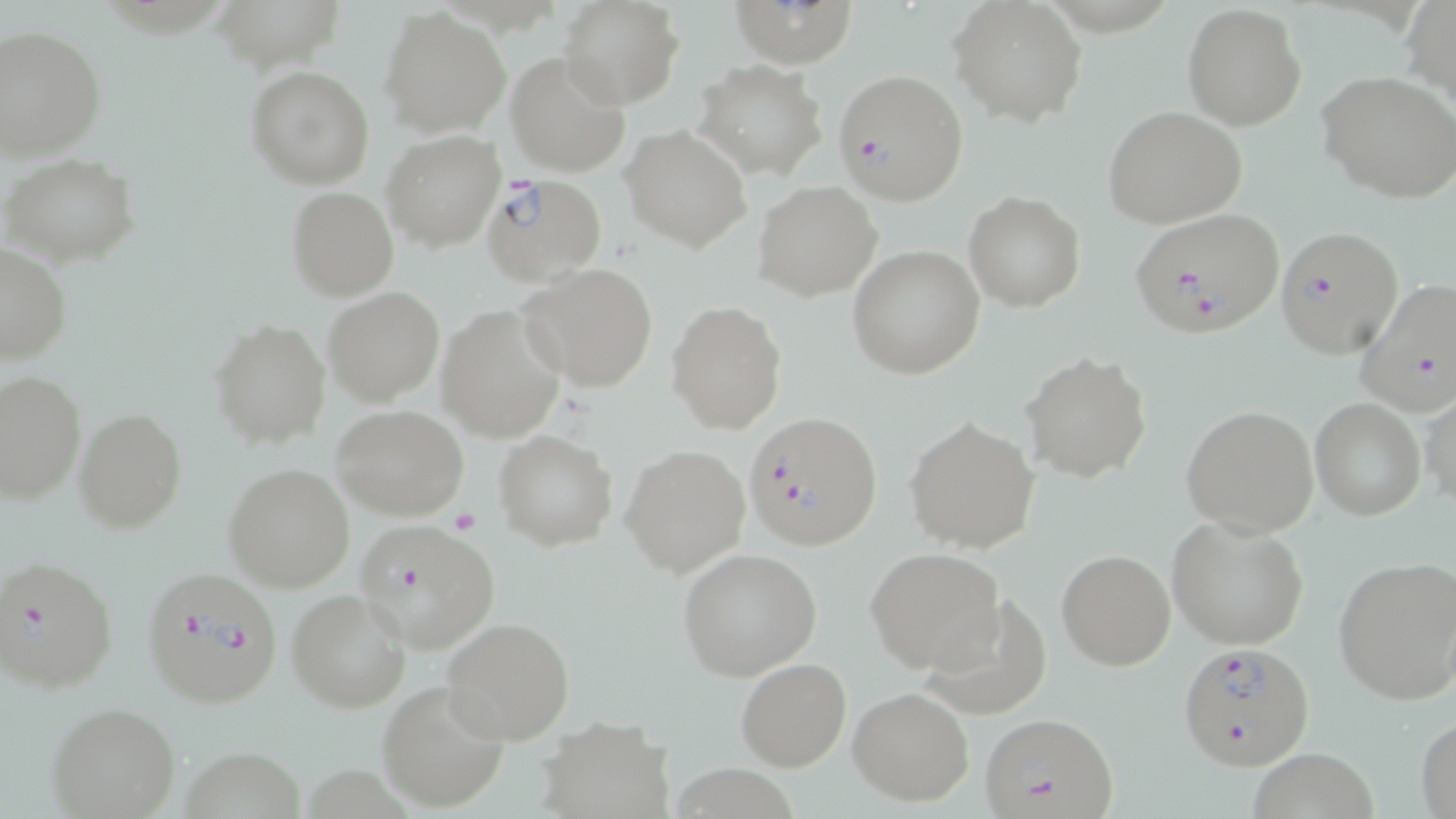

Approximate bounding boxes as [x1, y1, x2, y2] in pixels. Uninfected red blood cell locations: [559, 0, 682, 109], [733, 0, 854, 68], [948, 0, 1088, 128], [1404, 0, 1456, 116], [1182, 4, 1306, 131], [380, 6, 510, 137], [0, 25, 107, 160], [506, 51, 630, 178], [696, 59, 826, 180], [246, 64, 376, 189], [1317, 72, 1456, 203], [1102, 106, 1246, 228], [622, 125, 752, 253], [381, 130, 507, 251], [2, 153, 141, 268], [755, 182, 881, 301], [286, 186, 398, 301], [964, 192, 1086, 312], [0, 245, 72, 366], [847, 246, 985, 379], [522, 263, 660, 392], [323, 288, 445, 406], [666, 300, 786, 435], [437, 304, 565, 442], [211, 317, 330, 449], [1021, 353, 1152, 484], [1, 371, 85, 506], [1420, 392, 1456, 511], [1309, 397, 1427, 520], [332, 398, 469, 514], [1182, 405, 1319, 537], [74, 408, 187, 534], [904, 417, 1039, 554], [494, 430, 616, 552], [622, 444, 749, 578], [224, 464, 354, 592], [1167, 515, 1313, 650], [677, 547, 823, 681], [866, 548, 1005, 673], [1056, 549, 1175, 671], [1333, 558, 1456, 705], [286, 589, 411, 713], [927, 595, 1049, 717], [442, 616, 576, 744], [736, 657, 851, 771], [378, 679, 513, 812], [848, 687, 976, 806], [47, 702, 182, 819], [537, 716, 675, 819], [1416, 716, 1456, 817], [182, 743, 307, 819], [1249, 747, 1381, 819], [673, 759, 806, 819], [306, 760, 409, 819]. Plasmodium falciparum-infected red blood cell locations: [832, 69, 968, 204], [481, 174, 606, 288], [1128, 207, 1286, 338], [1274, 226, 1404, 360], [1357, 279, 1456, 416], [745, 410, 882, 551], [353, 521, 498, 653], [2, 555, 117, 696], [140, 564, 286, 710], [1177, 641, 1316, 771], [977, 711, 1119, 819]. Slide-level diagnosis: Plasmodium falciparum. Single field of view. May-Grünwald-Giemsa stain. 1000x magnification. Thin blood film. Optical microscopy. Image is 1456×819 pixels.